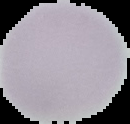

malaria status = uninfected
image type = segmented cell region on a black background
image size = 130×124 pixels
preparation = thin blood film